Locate and identify every blood parasite.
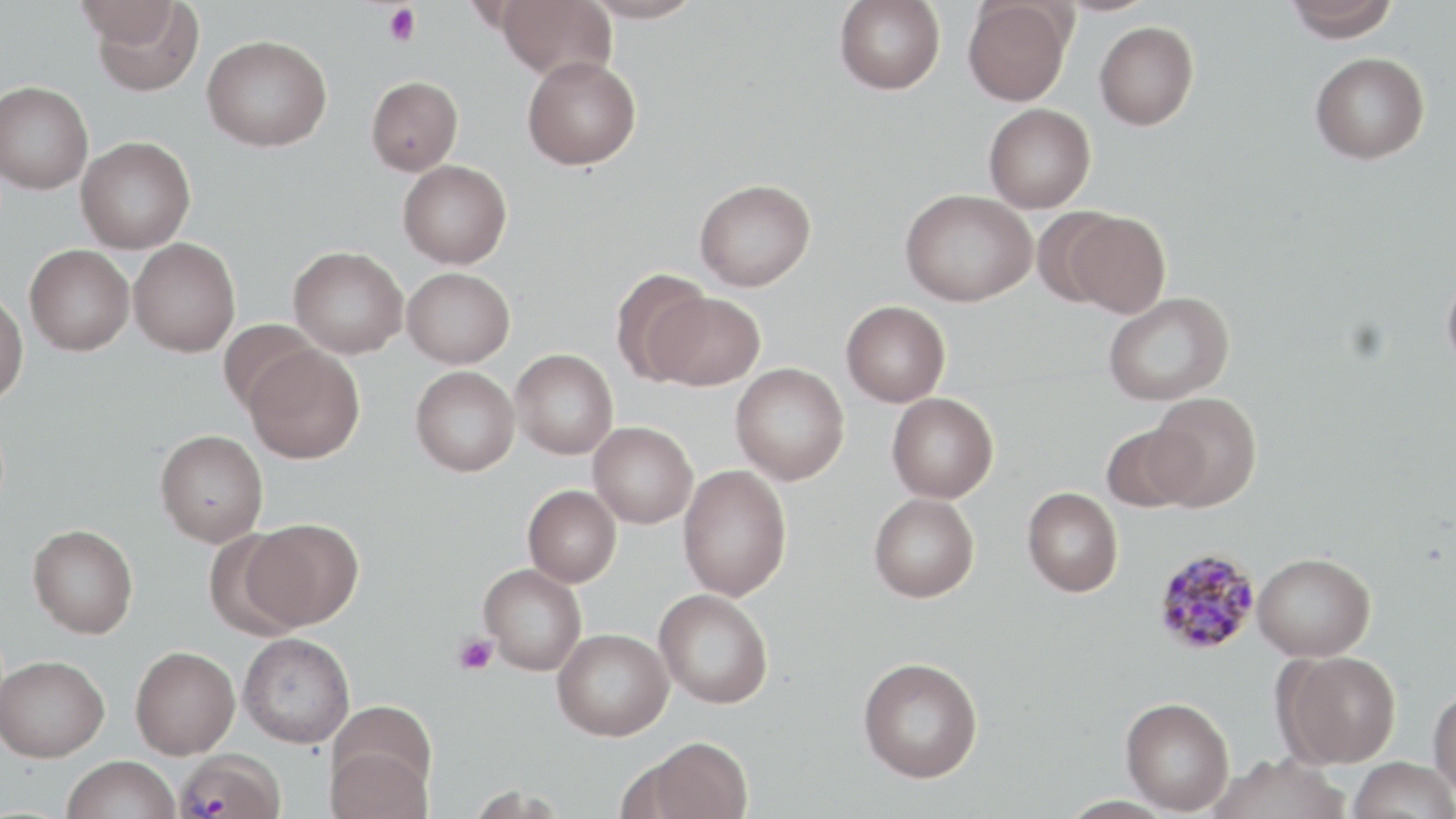
Approximate bounding boxes as (x1,y1)-(x2,y2) corner pairs in pixels.
Plasmodium malariae-infected red blood cells: (1154,547)-(1261,655), (176,750)-(286,819).
No Plasmodium falciparum, Plasmodium ovale, Plasmodium vivax, Babesia divergens, or Trypanosoma brucei observed.

slide-level diagnosis = Plasmodium malariae
field of view = one of a larger specimen
preparation = thin blood smear
stain = May-Grünwald-Giemsa
magnification = 1000x
image size = 1456×819 pixels
platelet locations = approximate bounding boxes as (x1,y1)-(x2,y2) corner pairs in pixels: (383,4)-(422,47), (453,634)-(498,675)
modality = light microscopy
uninfected red blood cell locations = approximate bounding boxes as (x1,y1)-(x2,y2) corner pairs in pixels: (75,0)-(183,48), (495,0)-(617,82), (582,0)-(705,24), (834,0)-(945,94), (1284,0)-(1400,42), (90,1)-(206,98), (963,1)-(1073,106), (1094,21)-(1199,130), (202,34)-(331,151), (1310,51)-(1430,164), (522,55)-(642,170), (366,76)-(463,175), (0,80)-(94,194), (984,103)-(1096,213), (76,135)-(196,253), (398,159)-(512,269), (694,178)-(816,291), (900,188)-(1037,306), (1032,207)-(1127,306), (1063,211)-(1170,318), (129,238)-(240,357), (25,244)-(134,355), (288,245)-(408,358), (1441,265)-(1456,381), (402,267)-(515,368), (609,268)-(712,384), (0,290)-(28,406), (1103,291)-(1235,406), (651,292)-(765,391), (841,300)-(951,407), (218,318)-(321,415), (245,346)-(364,464), (510,348)-(619,459), (730,363)-(850,485), (410,365)-(520,476), (1148,391)-(1262,511), (886,392)-(999,503), (588,421)-(698,528), (1101,423)-(1200,513), (155,430)-(269,547), (678,464)-(792,602), (522,484)-(622,587), (1022,487)-(1124,597), (869,492)-(980,602), (243,517)-(364,631), (28,524)-(138,638), (201,528)-(307,640), (1253,552)-(1376,661), (479,564)-(587,675), (654,589)-(774,709), (552,627)-(673,741), (238,632)-(355,748), (130,646)-(240,759), (1276,650)-(1401,768), (1,655)-(109,762), (858,657)-(983,782), (1429,687)-(1456,798), (1120,696)-(1235,814), (635,736)-(753,819), (325,743)-(433,819), (1210,753)-(1351,818), (62,755)-(181,819), (1348,756)-(1456,819)